Assess the morphology of the red blood cells.
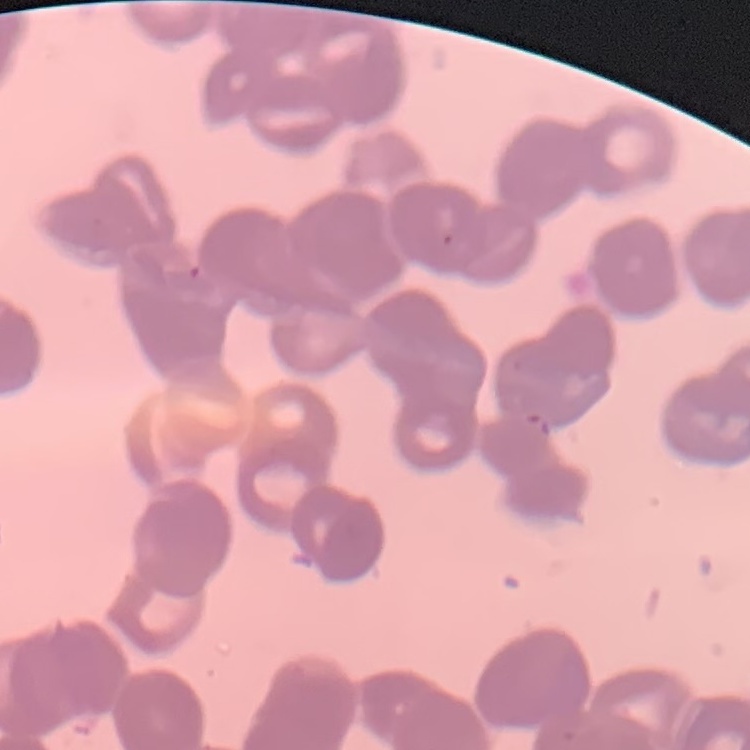

They show rouleaux formation.

Summary:
  - Stain: Field's or Giemsa
  - Image type: square crop of a larger photomicrograph
  - Preparation: thin blood smear